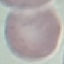 Malaria status: uninfected. Giemsa-stained preparation. Thin smear of blood. Automatically extracted cell patch, resized to 64 × 64 pixels. Photographed with a smartphone camera at the microscope eyepiece.